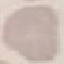 Result: no malaria parasites detected. Giemsa stain. Cell patch, automatically extracted from a larger field of view and resized to 64 × 64 pixels. Thin blood film. Photographed with a smartphone camera at the microscope eyepiece.